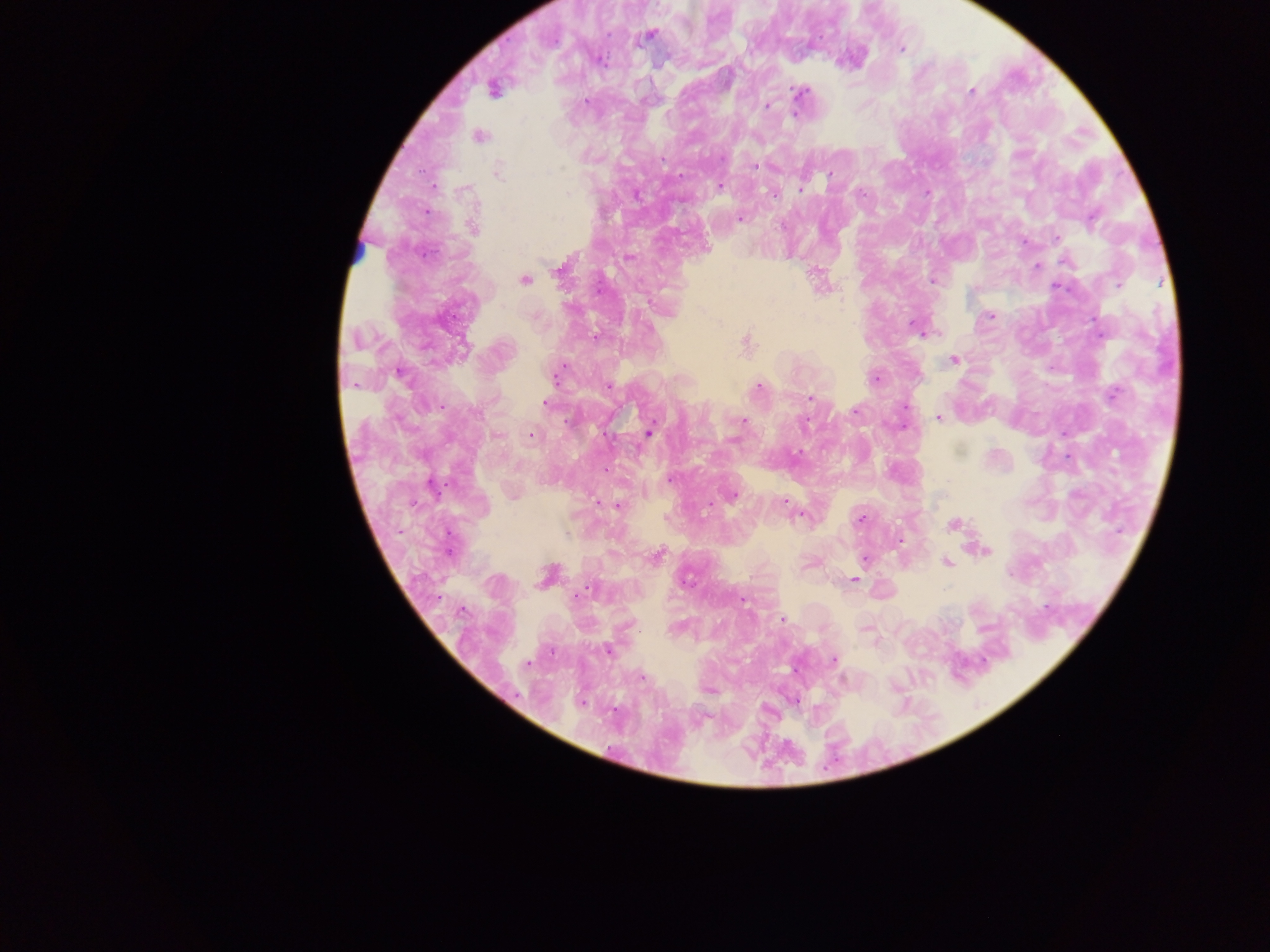

Approximate centers as x y in pixels.
Summary:
  - Malaria parasite locations: 648 36; 901 49; 493 88; 971 91; 800 93; 586 100; 766 106; 796 112; 477 136; 497 172; 718 185; 432 186; 800 190; 774 193; 739 218; 472 226; 1024 242; 629 258; 1066 260; 1036 266; 560 268; 524 279; 932 280; 990 315; 918 328; 926 333; 745 343; 954 360; 399 372; 555 375; 875 378; 608 385; 758 387; 1113 394; 810 398; 545 403; 905 407; 939 417; 742 421; 648 431; 530 435; 605 470; 669 478; 432 487; 512 492; 731 495; 709 503; 618 505; 802 514; 860 519; 954 525; 900 540; 981 549; 657 555; 864 558; 947 562; 548 575; 853 579; 742 598; 782 618; 867 629; 875 641; 607 650; 833 660; 641 677; 708 690; 793 700
  - Capture: mobile-phone photograph through a microscope
  - Country: Ghana
  - Preparation: thick blood film
  - Image size: 1270×952 pixels
  - Field of view: single